State which cell type is depicted.
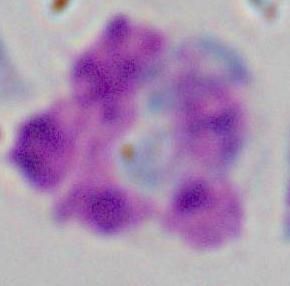

This is a leukocyte.

Captured at 1000x magnification. Micrograph.